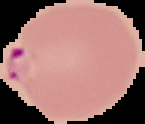
preparation = thin blood smear
image size = 145×124 pixels
result = Plasmodium parasites detected
image type = cell region segmented out of the field of view; surrounding area masked to black